Classify this cell by malaria status.
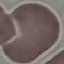
Uninfected.

preparation: thin blood film
image_type: cell patch, automatically extracted from a larger field of view and resized to 64 × 64 pixels
stain: Giemsa
capture: smartphone through the microscope eyepiece